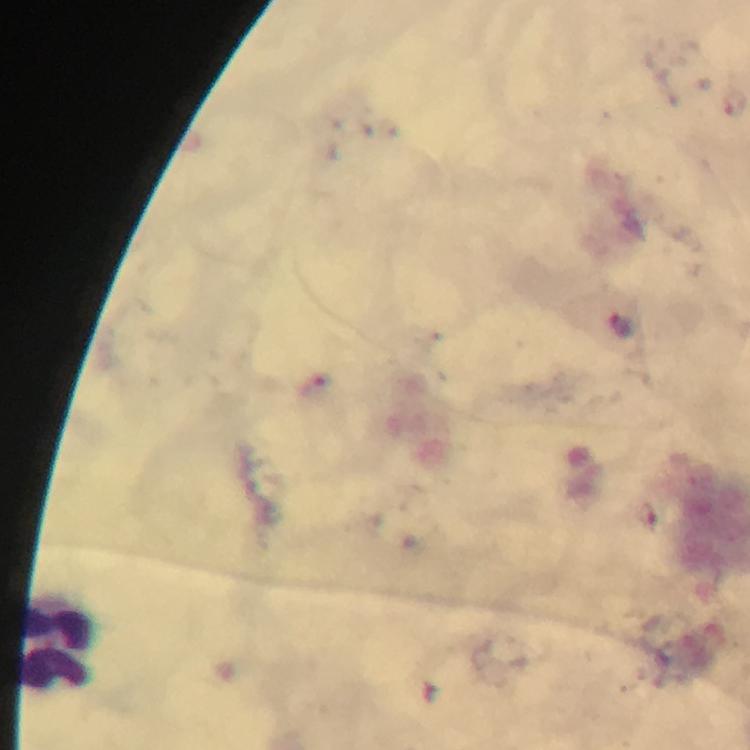
Approximate centers as [x, y] in pixels.
Summary:
  - Leukocyte locations: [56, 643]
  - Stain: Giemsa
  - Immersion oil: used
  - Cropped from: one field of view
  - Context: from a diagnostic examination for malaria
  - Magnification: 100x
  - Preparation: thick blood film
  - Capture: smartphone mounted on the microscope
  - Image size: 750×750 pixels
  - Malaria parasites: none detected